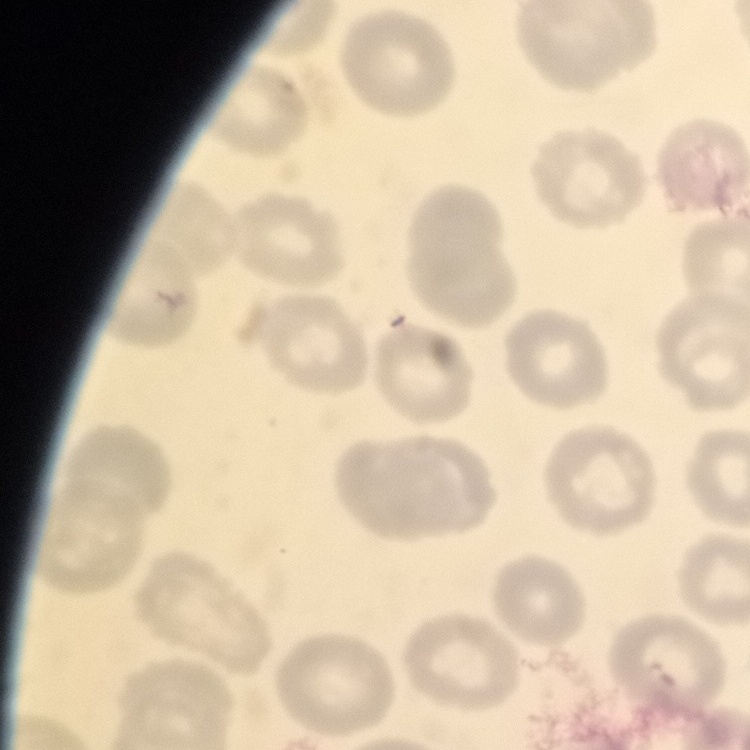
The red blood cells show no rouleaux formation. Thin blood smear. Stained with either Field's or Giemsa. Square crop of a larger photomicrograph.